Locate every blood parasite and identify its species.
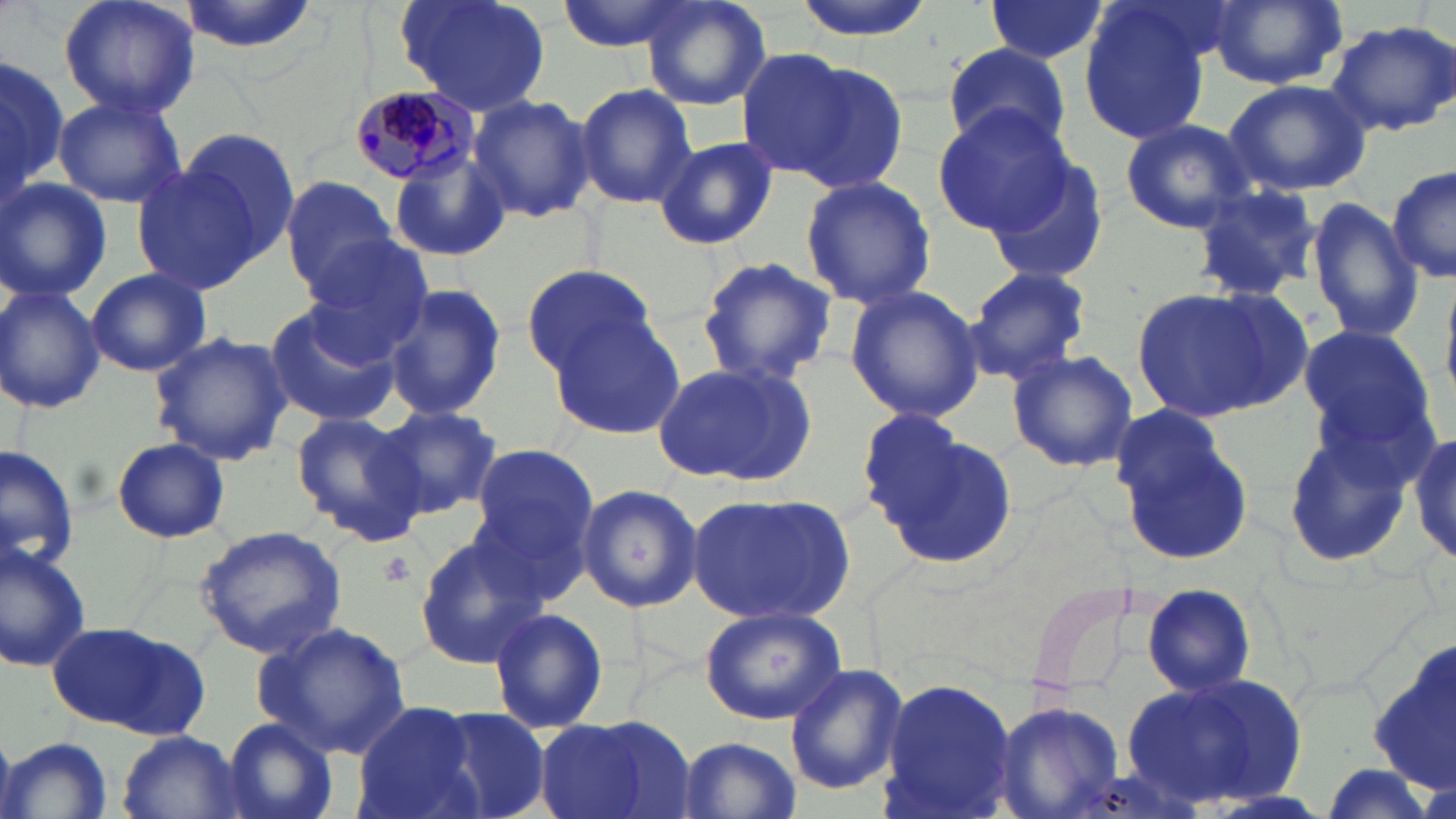
Approximate bounding boxes as named x1/y1/x2/y2 corners in pixels.
Plasmodium malariae-infected red blood cells: (x1=345, y1=85, x2=478, y2=188).
No Plasmodium falciparum, Plasmodium ovale, Plasmodium vivax, Babesia divergens, or Trypanosoma brucei observed.

Summary:
  - Platelet locations: (x1=380, y1=551, x2=415, y2=586)
  - Uninfected red blood cell locations: (x1=57, y1=0, x2=199, y2=120), (x1=175, y1=0, x2=323, y2=58), (x1=395, y1=0, x2=552, y2=118), (x1=556, y1=0, x2=694, y2=51), (x1=639, y1=0, x2=776, y2=110), (x1=790, y1=0, x2=933, y2=41), (x1=983, y1=0, x2=1108, y2=64), (x1=1202, y1=0, x2=1352, y2=90), (x1=1079, y1=4, x2=1214, y2=144), (x1=1322, y1=18, x2=1456, y2=137), (x1=944, y1=43, x2=1072, y2=155), (x1=733, y1=47, x2=851, y2=176), (x1=0, y1=53, x2=67, y2=205), (x1=784, y1=60, x2=910, y2=196), (x1=1225, y1=79, x2=1372, y2=197), (x1=576, y1=82, x2=697, y2=210), (x1=468, y1=92, x2=596, y2=224), (x1=52, y1=93, x2=188, y2=209), (x1=932, y1=106, x2=1077, y2=235), (x1=1120, y1=119, x2=1256, y2=233), (x1=177, y1=128, x2=301, y2=268), (x1=655, y1=135, x2=778, y2=250), (x1=389, y1=148, x2=511, y2=262), (x1=979, y1=150, x2=1112, y2=283), (x1=130, y1=163, x2=266, y2=297), (x1=1388, y1=163, x2=1455, y2=285), (x1=798, y1=173, x2=938, y2=310), (x1=280, y1=177, x2=401, y2=294), (x1=0, y1=178, x2=111, y2=304), (x1=1187, y1=182, x2=1325, y2=300), (x1=277, y1=184, x2=410, y2=417), (x1=1304, y1=197, x2=1424, y2=344), (x1=309, y1=235, x2=437, y2=361), (x1=695, y1=256, x2=840, y2=387), (x1=521, y1=262, x2=660, y2=377), (x1=963, y1=265, x2=1093, y2=385), (x1=85, y1=267, x2=210, y2=377), (x1=381, y1=281, x2=508, y2=421), (x1=843, y1=284, x2=984, y2=424), (x1=1134, y1=284, x2=1307, y2=424), (x1=0, y1=286, x2=105, y2=414), (x1=262, y1=305, x2=404, y2=427), (x1=548, y1=311, x2=687, y2=444), (x1=1294, y1=321, x2=1436, y2=459), (x1=149, y1=331, x2=294, y2=467), (x1=1006, y1=350, x2=1138, y2=471), (x1=653, y1=358, x2=820, y2=486), (x1=373, y1=404, x2=503, y2=520), (x1=1111, y1=410, x2=1253, y2=566), (x1=291, y1=411, x2=424, y2=539), (x1=870, y1=423, x2=1018, y2=573), (x1=1408, y1=423, x2=1456, y2=571), (x1=1280, y1=424, x2=1415, y2=569), (x1=112, y1=437, x2=231, y2=543), (x1=469, y1=443, x2=599, y2=573), (x1=1, y1=444, x2=80, y2=573), (x1=576, y1=482, x2=704, y2=613), (x1=689, y1=490, x2=856, y2=624), (x1=194, y1=525, x2=347, y2=657), (x1=412, y1=534, x2=546, y2=668), (x1=0, y1=536, x2=95, y2=672), (x1=1139, y1=583, x2=1257, y2=697), (x1=700, y1=605, x2=847, y2=725), (x1=487, y1=606, x2=609, y2=735), (x1=254, y1=621, x2=412, y2=759), (x1=50, y1=622, x2=207, y2=739), (x1=1364, y1=639, x2=1456, y2=791), (x1=785, y1=663, x2=908, y2=796), (x1=1121, y1=668, x2=1310, y2=810), (x1=877, y1=675, x2=1018, y2=819), (x1=990, y1=701, x2=1124, y2=819), (x1=352, y1=702, x2=484, y2=819), (x1=433, y1=706, x2=555, y2=819), (x1=535, y1=716, x2=696, y2=819), (x1=221, y1=718, x2=342, y2=819), (x1=116, y1=732, x2=244, y2=818), (x1=675, y1=735, x2=799, y2=819), (x1=4, y1=736, x2=113, y2=819)
  - Slide-level diagnosis: Plasmodium malariae
  - Field of view: single
  - Modality: light microscopy
  - Magnification: 1000x
  - Image size: 1456×819 pixels
  - Preparation: thin blood smear
  - Stain: May-Grünwald-Giemsa